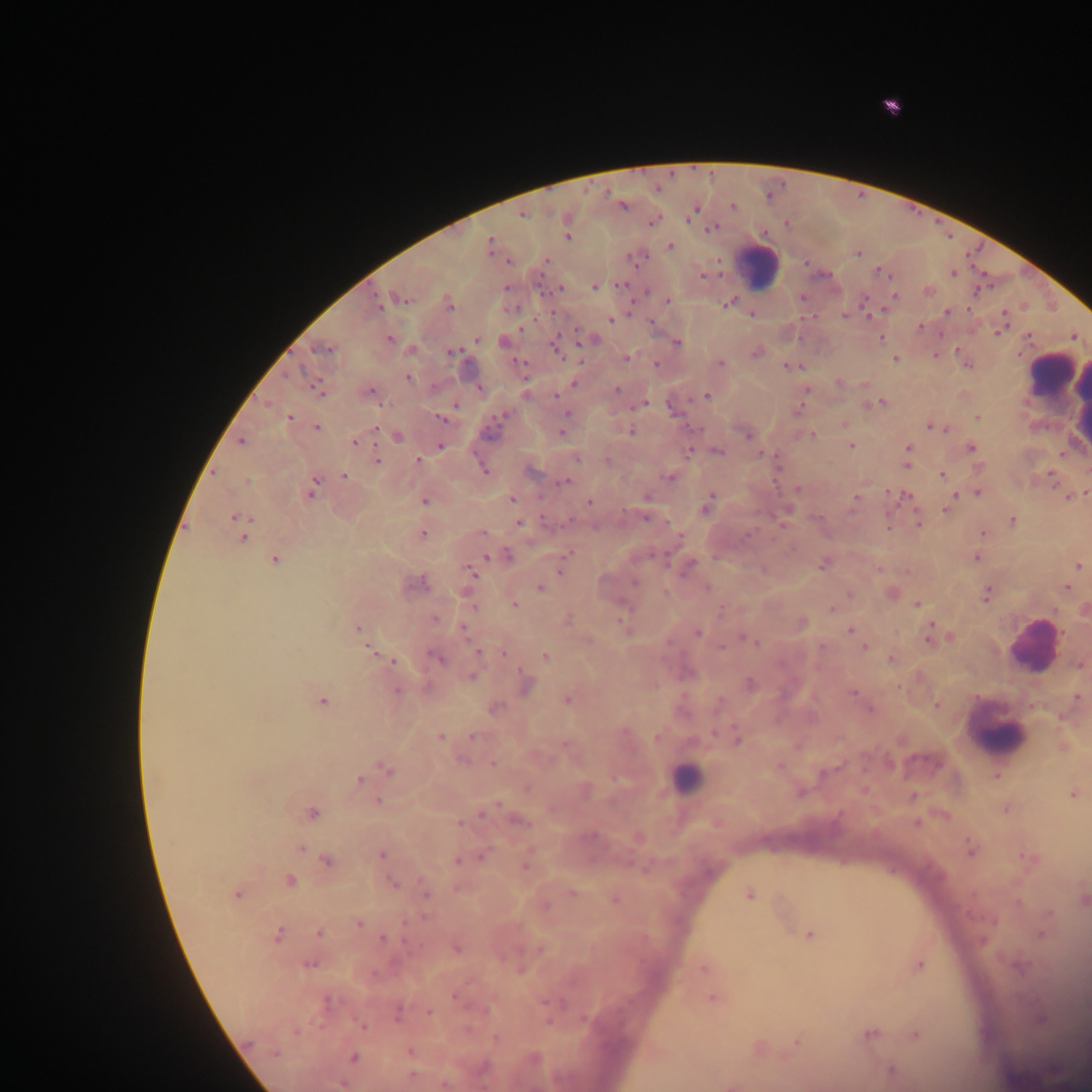

Approximate centers as (x, y) in pixels.
Summary:
  - Leukocyte locations: (757, 267), (1050, 373), (1056, 391), (1033, 648), (999, 734), (684, 779)
  - Plasmodium parasite locations: (623, 205), (734, 206), (693, 209), (521, 213), (653, 221), (711, 228), (567, 236), (489, 245), (669, 246), (857, 252), (545, 261), (953, 272), (595, 286), (559, 289), (928, 291), (894, 295), (401, 298), (666, 300), (729, 302), (377, 303), (449, 304), (946, 312), (751, 314), (844, 316), (611, 319), (920, 326), (1001, 328), (476, 338), (881, 338), (389, 339), (591, 339), (504, 342), (676, 342), (324, 347), (556, 347), (958, 351), (452, 352), (755, 352), (626, 358), (895, 359), (720, 364), (656, 365), (790, 366), (407, 377), (574, 383), (838, 383), (318, 387), (616, 390), (806, 391), (369, 393), (707, 395), (879, 402), (640, 403), (671, 406), (441, 416), (289, 417), (566, 417), (978, 417), (843, 424), (933, 426), (316, 427), (941, 428), (562, 430), (629, 430), (748, 434), (810, 435), (396, 437), (241, 440), (354, 441), (850, 445), (440, 446), (970, 447), (908, 449), (715, 450), (688, 452), (761, 453), (575, 457), (377, 461), (418, 461), (906, 464), (979, 467), (482, 469), (532, 471), (942, 475), (344, 476), (669, 476), (564, 482), (311, 488), (797, 489), (978, 492), (1085, 493), (953, 494), (896, 495), (1069, 496), (647, 497), (855, 497), (512, 498), (424, 499), (589, 503), (708, 503), (947, 508), (787, 510), (235, 517), (917, 521), (1012, 521), (519, 522), (887, 526), (983, 533), (423, 534), (243, 537), (569, 551), (498, 555), (975, 557), (274, 559), (823, 563), (688, 565), (1078, 566), (877, 568), (560, 569), (470, 572), (414, 583), (540, 588), (1067, 588), (849, 593), (891, 593), (986, 594), (514, 604), (917, 604), (832, 608), (1083, 610), (434, 619), (566, 619), (622, 622), (801, 623), (358, 629), (851, 630), (698, 633), (930, 635), (946, 637), (746, 639), (721, 646), (863, 647), (371, 649), (478, 651), (504, 653), (437, 657), (545, 657), (891, 659), (392, 660), (1080, 663), (471, 676), (525, 683), (749, 684), (396, 690), (853, 693), (567, 698), (1076, 698), (322, 700), (937, 704), (494, 707), (869, 708), (472, 736), (440, 737), (736, 739), (1062, 746), (493, 763), (778, 767), (387, 770), (361, 779), (800, 791), (1073, 793), (377, 801), (1006, 807), (486, 810), (311, 813), (516, 820), (637, 838), (300, 849), (970, 849), (381, 854), (482, 855), (1029, 858), (458, 860), (326, 861), (525, 865), (288, 881), (392, 883), (425, 891), (237, 893), (571, 893), (749, 894), (614, 899), (1081, 899), (544, 904), (358, 923), (1043, 925), (319, 932), (278, 934), (809, 934), (383, 939), (456, 948), (539, 949), (309, 963), (918, 964), (704, 967), (713, 997), (327, 1002), (397, 1012), (429, 1013), (1041, 1018), (362, 1026), (869, 1034), (914, 1034), (797, 1041), (758, 1048), (409, 1052), (353, 1057), (532, 1059), (891, 1070), (342, 1083), (444, 1083), (734, 1084)
  - Capture: mobile-phone photograph through a microscope
  - Country: Ghana
  - Preparation: thick blood smear
  - Field of view: single
  - Image size: 1092×1092 pixels